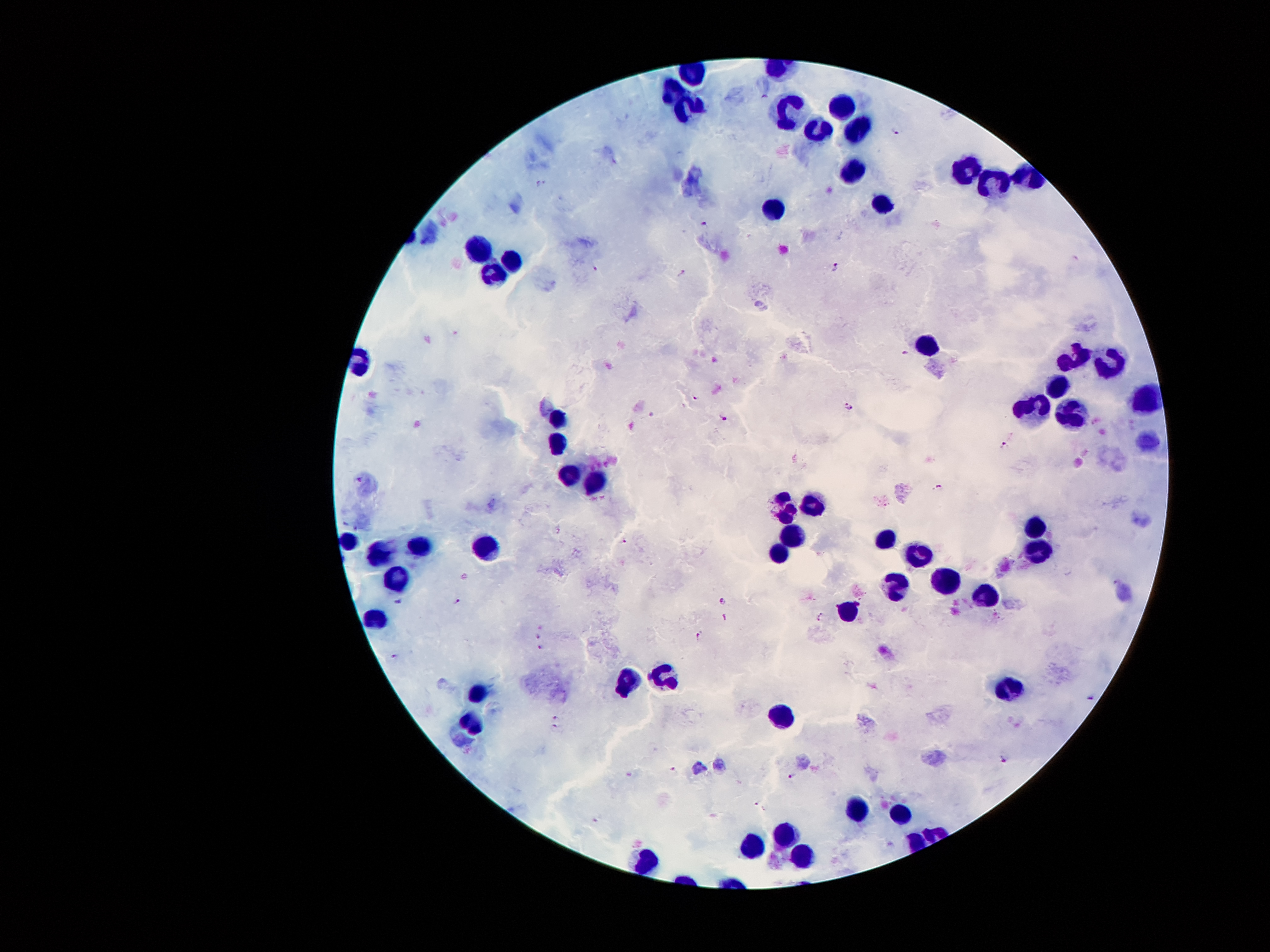
Approximate object centers, in pixels from the top-left corner. Malaria parasite locations: (x=897, y=131), (x=543, y=184), (x=705, y=225), (x=598, y=267), (x=836, y=267), (x=682, y=273), (x=905, y=354), (x=695, y=398), (x=847, y=406), (x=725, y=418), (x=1005, y=445), (x=360, y=479), (x=938, y=487), (x=624, y=542), (x=398, y=601), (x=457, y=601), (x=724, y=601), (x=725, y=617), (x=822, y=617), (x=539, y=627), (x=538, y=636), (x=698, y=637), (x=540, y=648), (x=397, y=658), (x=1091, y=696), (x=556, y=717), (x=555, y=728), (x=1006, y=759), (x=674, y=771), (x=630, y=774), (x=792, y=774), (x=757, y=804). Leukocyte locations: (x=671, y=84), (x=684, y=106), (x=785, y=107), (x=842, y=107), (x=860, y=121), (x=814, y=131), (x=965, y=166), (x=850, y=176), (x=991, y=185), (x=884, y=204), (x=772, y=208), (x=479, y=244), (x=513, y=261), (x=492, y=271), (x=930, y=338), (x=1073, y=355), (x=1110, y=363), (x=1055, y=383), (x=1143, y=400), (x=1031, y=405), (x=1071, y=410), (x=556, y=422), (x=556, y=442), (x=567, y=473), (x=595, y=476), (x=812, y=503), (x=786, y=504), (x=1034, y=523), (x=793, y=534), (x=885, y=538), (x=348, y=541), (x=1040, y=543), (x=419, y=544), (x=489, y=544), (x=779, y=547), (x=379, y=549), (x=919, y=550), (x=395, y=578), (x=941, y=579), (x=893, y=586), (x=985, y=597), (x=849, y=608), (x=374, y=617), (x=660, y=675), (x=626, y=682), (x=1006, y=691), (x=476, y=695), (x=775, y=713), (x=472, y=720), (x=855, y=807), (x=899, y=812), (x=785, y=830), (x=754, y=842), (x=799, y=855), (x=649, y=863). Thick peripheral-blood smear. Single field of view. Smartphone photograph taken through the microscope eyepiece. Giemsa-stained preparation. Image is 1270×952 pixels. Patient malaria status: positive for Plasmodium falciparum. 100x magnification.